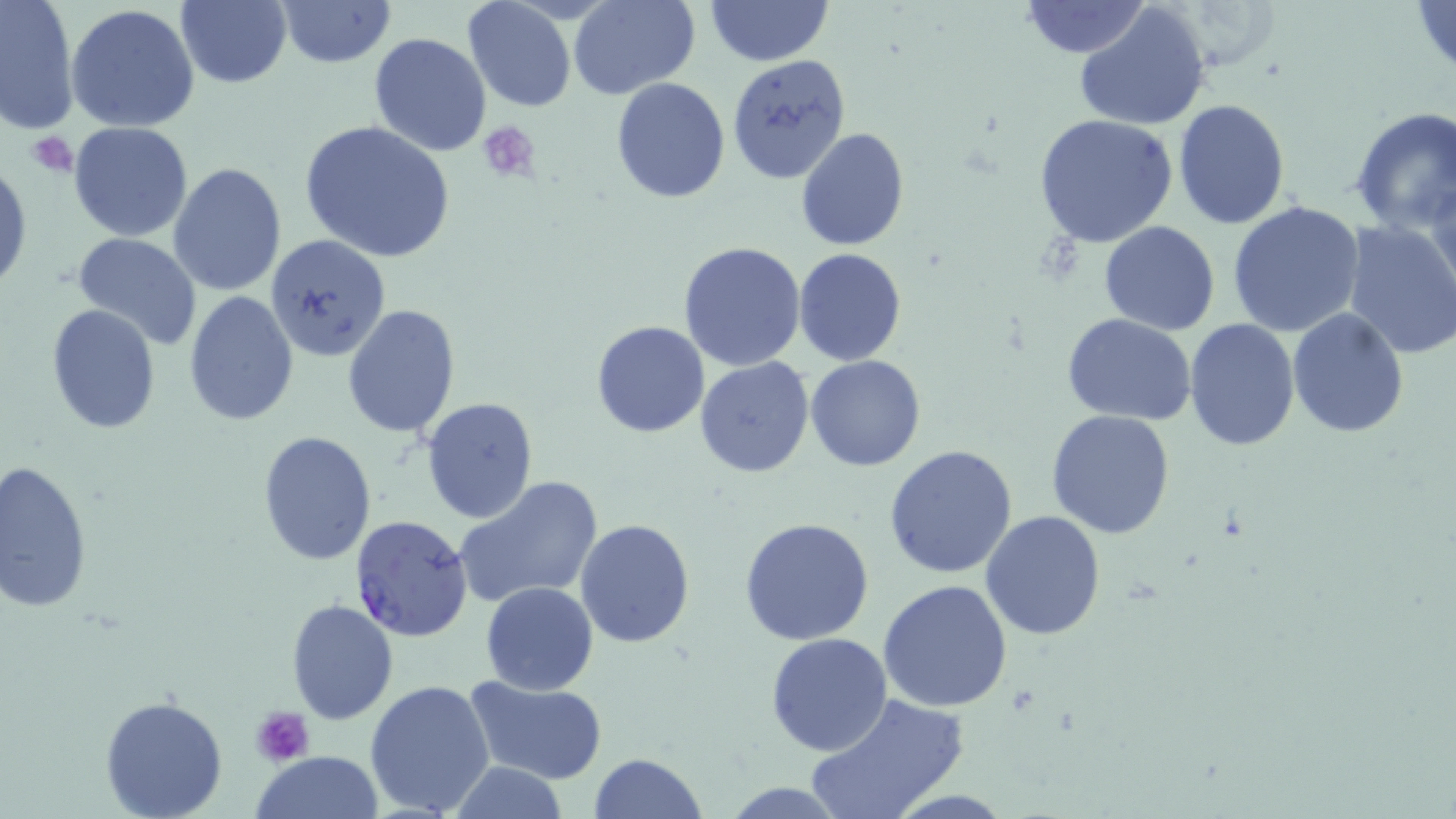

Summary:
  - Coordinate format: approximate bounding boxes as (x1, y1, x2, y2) in pixels
  - Plasmodium falciparum-infected red blood cell locations: (349, 513, 474, 643)
  - Platelet locations: (475, 120, 541, 181), (27, 132, 77, 176), (253, 707, 314, 768)
  - Uninfected red blood cell locations: (0, 0, 81, 135), (462, 0, 577, 113), (570, 0, 697, 99), (703, 0, 836, 66), (1411, 0, 1456, 78), (174, 1, 292, 88), (275, 1, 396, 69), (1018, 1, 1152, 58), (1074, 4, 1211, 132), (65, 5, 199, 132), (369, 32, 491, 156), (725, 51, 851, 181), (610, 77, 730, 204), (1173, 99, 1290, 229), (1348, 106, 1456, 235), (1035, 114, 1177, 249), (299, 119, 455, 262), (69, 121, 195, 241), (795, 128, 910, 250), (0, 160, 32, 296), (169, 163, 287, 297), (1426, 171, 1456, 307), (1227, 199, 1365, 337), (1099, 221, 1220, 335), (1340, 221, 1456, 361), (72, 231, 202, 351), (265, 233, 392, 362), (678, 241, 807, 372), (793, 249, 907, 365), (185, 292, 298, 428), (340, 303, 460, 440), (44, 304, 162, 432), (1286, 307, 1410, 437), (1062, 313, 1200, 424), (1185, 318, 1300, 450), (590, 321, 709, 437), (807, 356, 926, 473), (695, 357, 814, 478), (421, 398, 538, 522), (1047, 409, 1177, 540), (257, 431, 377, 565), (884, 445, 1019, 579), (1, 458, 95, 613), (455, 474, 604, 609), (981, 512, 1106, 642), (575, 518, 695, 650), (740, 519, 874, 644), (877, 579, 1014, 712), (480, 582, 599, 694), (286, 599, 398, 725), (765, 632, 892, 755), (464, 676, 608, 785), (364, 679, 497, 817), (99, 694, 229, 819), (806, 694, 968, 819), (251, 750, 383, 819), (587, 753, 709, 818), (446, 759, 569, 819), (718, 781, 852, 816)
  - Slide-level diagnosis: Plasmodium falciparum
  - Magnification: 1000x
  - Modality: light microscopy
  - Field of view: one of a larger specimen
  - Image size: 1456×819 pixels
  - Stain: May-Grünwald-Giemsa
  - Preparation: thin blood smear